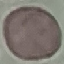

Malaria status: uninfected. Thin blood smear. Giemsa-stained preparation. Acquired by smartphone through the microscope eyepiece. Cell patch, automatically extracted from a larger field of view and resized to 64 × 64 pixels.